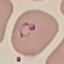
{
  "malaria_status": "parasitized",
  "stain": "Giemsa",
  "capture": "smartphone camera at the microscope eyepiece",
  "image_type": "automatically extracted cell patch, resized to 64 × 64 pixels",
  "preparation": "thin blood smear"
}